Outline each blood parasite and name the species.
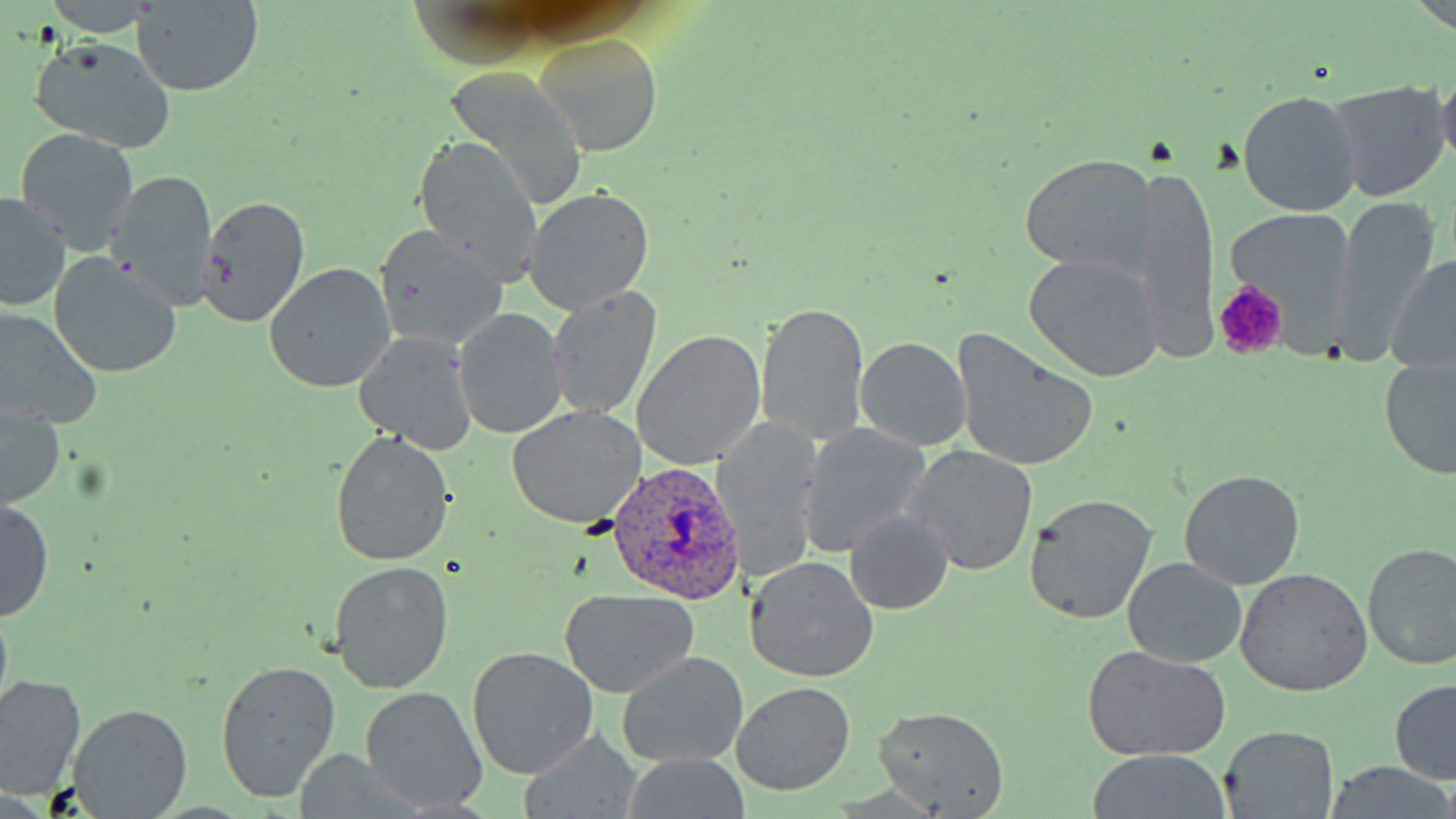

Approximate bounding boxes as named x1/y1/x2/y2 corners in pixels.
Plasmodium ovale-infected red blood cells: (x1=606, y1=457, x2=743, y2=605).
No Plasmodium falciparum, Plasmodium malariae, Plasmodium vivax, Babesia divergens, or Trypanosoma brucei observed.

slide_level_diagnosis: Plasmodium ovale
image_size: 1456×819 pixels
magnification: 1000x
modality: optical microscopy
platelet_locations: 'approximate bounding boxes as named x1/y1/x2/y2 corners in pixels: (x1=1212, y1=280, x2=1286, y2=359)'
stain: May-Grünwald-Giemsa
field_of_view: one of a larger specimen
preparation: thin blood smear
uninfected_red_blood_cell_locations: 'approximate bounding boxes as named x1/y1/x2/y2 corners in pixels: (x1=130, y1=2, x2=264, y2=96), (x1=536, y1=32, x2=666, y2=155), (x1=28, y1=35, x2=177, y2=156), (x1=442, y1=64, x2=589, y2=210), (x1=1324, y1=81, x2=1450, y2=205), (x1=1238, y1=90, x2=1364, y2=218), (x1=15, y1=129, x2=140, y2=253), (x1=412, y1=133, x2=544, y2=286), (x1=1020, y1=153, x2=1156, y2=278), (x1=1136, y1=164, x2=1219, y2=367), (x1=104, y1=170, x2=219, y2=308), (x1=523, y1=188, x2=653, y2=316), (x1=196, y1=191, x2=311, y2=330), (x1=0, y1=193, x2=71, y2=312), (x1=1332, y1=196, x2=1444, y2=355), (x1=1225, y1=211, x2=1353, y2=323), (x1=372, y1=223, x2=507, y2=352), (x1=1387, y1=250, x2=1456, y2=379), (x1=1023, y1=253, x2=1165, y2=384), (x1=48, y1=255, x2=182, y2=379), (x1=263, y1=262, x2=394, y2=394), (x1=548, y1=287, x2=663, y2=420), (x1=755, y1=298, x2=870, y2=448), (x1=0, y1=309, x2=100, y2=433), (x1=455, y1=311, x2=569, y2=438), (x1=950, y1=329, x2=1101, y2=474), (x1=631, y1=330, x2=767, y2=470), (x1=354, y1=332, x2=477, y2=457), (x1=855, y1=337, x2=971, y2=452), (x1=1381, y1=356, x2=1456, y2=480), (x1=1, y1=400, x2=65, y2=511), (x1=507, y1=405, x2=643, y2=529), (x1=717, y1=417, x2=823, y2=581), (x1=800, y1=424, x2=932, y2=557), (x1=331, y1=430, x2=454, y2=566), (x1=905, y1=444, x2=1038, y2=577), (x1=1178, y1=469, x2=1305, y2=590), (x1=1196, y1=474, x2=1334, y2=663), (x1=1024, y1=493, x2=1156, y2=626), (x1=0, y1=498, x2=54, y2=622), (x1=844, y1=510, x2=954, y2=614), (x1=1361, y1=541, x2=1456, y2=672), (x1=744, y1=556, x2=879, y2=682), (x1=1123, y1=557, x2=1247, y2=669), (x1=329, y1=561, x2=455, y2=693), (x1=1235, y1=568, x2=1372, y2=696), (x1=557, y1=589, x2=699, y2=698), (x1=1082, y1=645, x2=1232, y2=762), (x1=468, y1=647, x2=597, y2=778), (x1=618, y1=651, x2=749, y2=769), (x1=215, y1=658, x2=342, y2=804), (x1=0, y1=674, x2=84, y2=803), (x1=1390, y1=679, x2=1456, y2=784), (x1=732, y1=682, x2=856, y2=797), (x1=361, y1=686, x2=487, y2=812), (x1=71, y1=702, x2=193, y2=817), (x1=872, y1=705, x2=1008, y2=816), (x1=1219, y1=727, x2=1340, y2=818), (x1=1084, y1=752, x2=1234, y2=819), (x1=1324, y1=763, x2=1456, y2=817)'